State the blood parasite species.
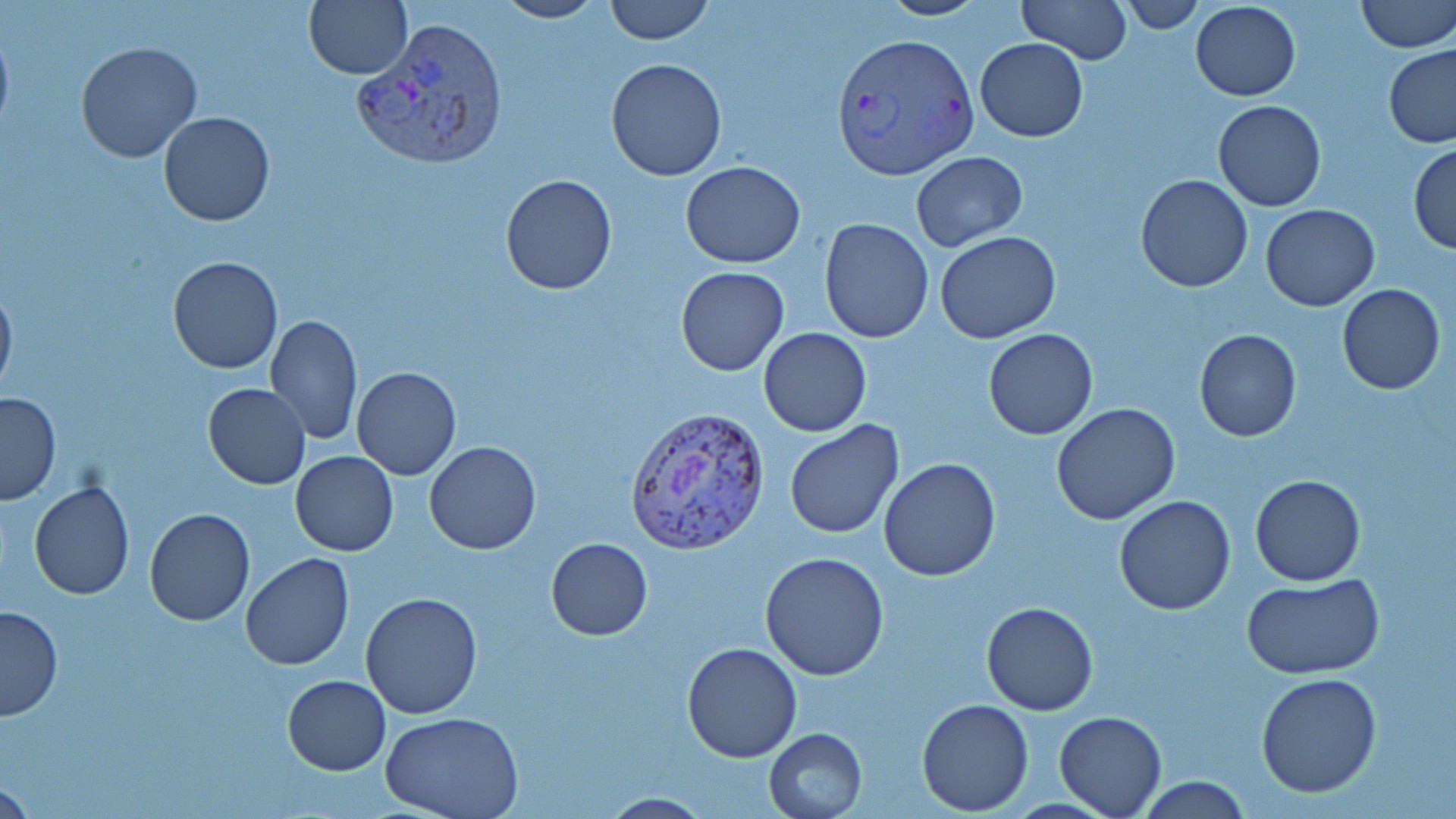

Plasmodium vivax.

Approximate bounding boxes as (x1, y1, x2, y2) in pixels. Uninfected red blood cell locations: (304, 0, 412, 80), (491, 0, 608, 24), (603, 0, 714, 45), (876, 0, 992, 21), (1016, 0, 1129, 64), (1356, 0, 1455, 53), (1119, 1, 1206, 32), (1190, 1, 1301, 101), (0, 20, 14, 141), (975, 38, 1089, 141), (75, 42, 203, 163), (1384, 44, 1456, 147), (605, 58, 727, 181), (1212, 100, 1326, 212), (157, 112, 274, 227), (1408, 143, 1456, 254), (910, 151, 1028, 251), (680, 161, 805, 268), (500, 174, 617, 294), (1137, 175, 1253, 292), (1261, 203, 1379, 310), (819, 218, 934, 342), (934, 232, 1060, 344), (168, 257, 282, 373), (675, 266, 789, 376), (0, 278, 17, 397), (1337, 284, 1444, 396), (266, 315, 362, 444), (758, 328, 871, 437), (983, 329, 1099, 440), (1194, 330, 1302, 442), (352, 366, 460, 480), (204, 383, 311, 489), (0, 392, 62, 504), (1050, 402, 1180, 525), (784, 421, 906, 538), (424, 441, 541, 554), (291, 451, 399, 557), (879, 458, 1001, 581), (1250, 475, 1365, 586), (27, 482, 134, 600), (1114, 495, 1237, 615), (144, 508, 256, 627), (545, 538, 653, 640), (760, 551, 890, 681), (240, 554, 354, 671), (1242, 573, 1385, 680), (360, 592, 485, 720), (981, 602, 1100, 715), (0, 604, 63, 721), (680, 642, 803, 763), (1255, 671, 1383, 797), (283, 675, 391, 774), (917, 698, 1034, 815), (380, 709, 524, 819), (1055, 712, 1166, 818), (764, 728, 868, 818), (1135, 776, 1253, 817), (596, 793, 715, 818). Plasmodium vivax-infected red blood cell locations: (350, 21, 512, 166), (831, 30, 976, 178), (624, 404, 771, 554). May-Grünwald-Giemsa-stained preparation. Thin blood smear. One field of a larger specimen. Image is 1456×819 pixels. 1000x magnification. Optical microscopy.